Locate every Plasmodium malariae-infected red blood cell.
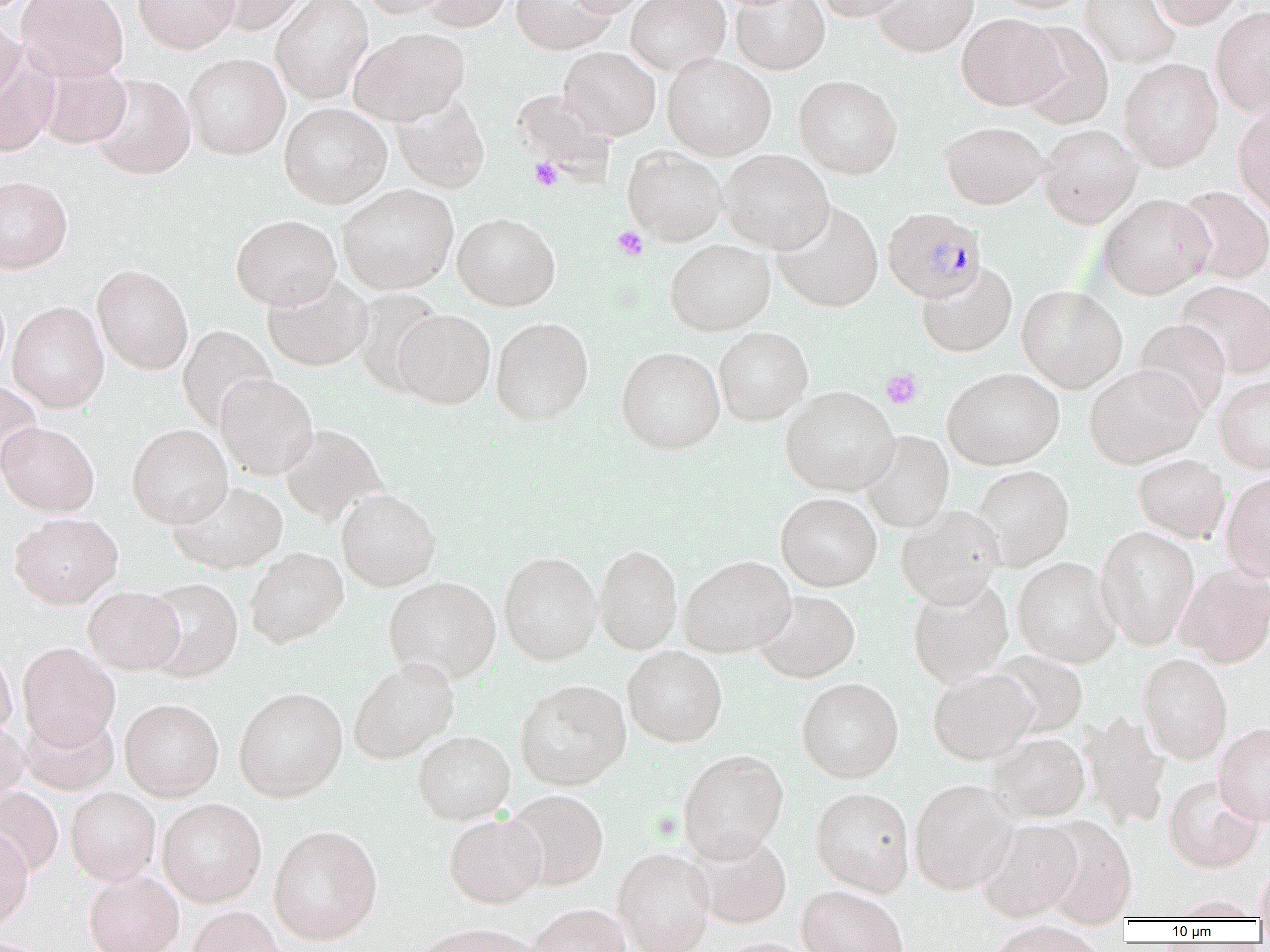

Approximate bounding boxes as [x1, y1, x2, y2] in pixels.
Plasmodium malariae-infected red blood cells: [882, 207, 987, 303].

Platelet locations: [529, 157, 563, 191], [613, 226, 648, 260], [881, 368, 922, 409]. Uninfected red blood cell locations: [17, 0, 129, 81], [133, 0, 239, 53], [203, 0, 314, 35], [271, 0, 373, 104], [357, 0, 455, 18], [420, 0, 514, 32], [511, 0, 616, 55], [565, 0, 653, 17], [626, 0, 730, 75], [731, 0, 829, 74], [813, 0, 912, 21], [873, 0, 978, 57], [992, 0, 1092, 14], [1080, 0, 1180, 68], [1150, 0, 1244, 29], [1211, 5, 1270, 116], [0, 13, 23, 104], [957, 13, 1064, 110], [1016, 22, 1114, 130], [350, 27, 469, 125], [559, 47, 660, 140], [0, 48, 60, 157], [183, 53, 290, 159], [662, 53, 776, 160], [1119, 58, 1223, 172], [34, 59, 132, 149], [89, 74, 196, 180], [794, 75, 902, 178], [512, 89, 617, 180], [390, 94, 490, 194], [279, 102, 391, 209], [1233, 103, 1270, 217], [939, 121, 1048, 209], [1038, 123, 1143, 229], [623, 146, 726, 245], [718, 149, 834, 254], [0, 175, 73, 273], [337, 184, 458, 294], [1175, 185, 1270, 284], [1098, 194, 1214, 299], [772, 201, 883, 313], [452, 212, 560, 311], [231, 214, 340, 310], [665, 239, 775, 336], [91, 263, 194, 374], [916, 263, 1017, 358], [263, 273, 373, 371], [1176, 281, 1270, 379], [1017, 285, 1127, 393], [352, 288, 445, 394], [7, 301, 109, 413], [393, 309, 496, 409], [491, 316, 594, 426], [1133, 319, 1230, 419], [178, 325, 275, 429], [714, 326, 813, 425], [616, 347, 725, 454], [1084, 365, 1204, 469], [942, 368, 1064, 470], [215, 374, 319, 479], [1214, 377, 1270, 474], [0, 380, 44, 475], [780, 386, 899, 495], [0, 421, 100, 517], [127, 424, 232, 528], [279, 424, 386, 525], [859, 431, 954, 533], [1133, 455, 1230, 543], [971, 466, 1074, 571], [1221, 474, 1270, 583], [168, 480, 288, 574], [336, 488, 441, 591], [776, 492, 882, 591], [896, 505, 1005, 609], [9, 513, 122, 608], [1096, 527, 1200, 648], [595, 544, 682, 655], [245, 547, 348, 648], [498, 551, 602, 665], [679, 555, 795, 657], [1012, 557, 1122, 668], [1175, 565, 1270, 668], [383, 576, 501, 684], [142, 577, 244, 682], [908, 578, 1013, 688], [83, 586, 184, 674], [754, 591, 860, 683], [17, 642, 120, 749], [622, 646, 727, 748], [0, 648, 17, 740], [987, 651, 1088, 738], [1138, 654, 1233, 764], [348, 658, 459, 764], [928, 669, 1038, 765], [796, 678, 903, 783], [515, 679, 631, 790], [234, 686, 348, 802], [120, 698, 224, 801], [20, 710, 119, 795], [1079, 712, 1170, 829], [0, 719, 30, 810], [1214, 722, 1270, 826], [413, 730, 515, 825], [986, 733, 1090, 822], [678, 749, 789, 863], [1163, 775, 1265, 872], [909, 780, 1019, 894], [0, 786, 63, 877], [66, 787, 161, 886], [810, 787, 915, 896], [504, 790, 609, 891], [157, 799, 267, 907], [444, 813, 547, 909], [1039, 817, 1137, 927], [977, 819, 1084, 922], [0, 825, 33, 931], [269, 825, 382, 946], [688, 831, 792, 929], [612, 848, 715, 952], [1255, 859, 1270, 924], [84, 871, 184, 952], [797, 886, 908, 952], [1167, 894, 1263, 921], [527, 904, 632, 952], [187, 906, 286, 952], [984, 922, 1110, 952], [415, 923, 539, 952], [711, 938, 817, 952]. Slide-level diagnosis: Plasmodium malariae. Thin blood film. Captured at 1000x magnification. Image is 1270×952 pixels. Light microscopy. One field of a larger specimen.